Assess this cell for malaria.
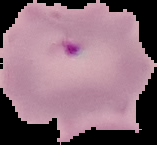

It is parasitized.

Summary:
  - Preparation: thin blood film
  - Image type: segmented cell region on a black background
  - Image size: 157×145 pixels